Report the malaria status of this cell.
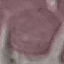
Uninfected.

Thin blood film. Automatically extracted cell patch, resized to 64 × 64 pixels. Acquired by smartphone through the microscope eyepiece. Giemsa stain.